Outline each blood parasite and name the species.
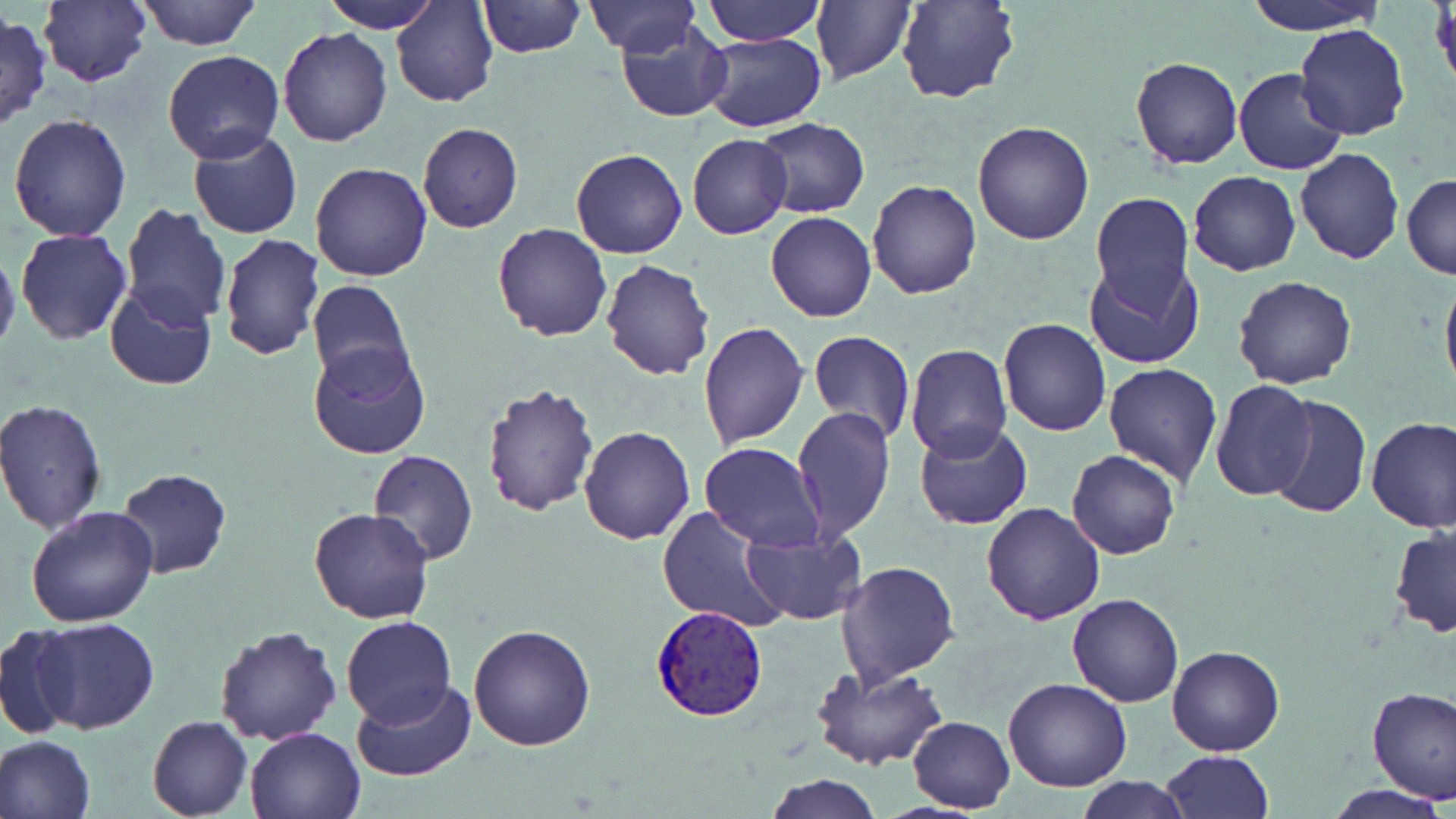
Approximate bounding boxes as (x1, y1, x2, y2) in pixels.
Plasmodium vivax-infected red blood cells: (649, 605, 770, 721).
No Plasmodium falciparum, Plasmodium ovale, Plasmodium malariae, Babesia divergens, or Trypanosoma brucei observed.

slide-level diagnosis = Plasmodium vivax
uninfected red blood cell locations = approximate bounding boxes as (x1, y1, x2, y2) in pixels: (134, 0, 263, 50), (322, 0, 440, 33), (393, 0, 497, 106), (477, 0, 586, 56), (703, 0, 825, 46), (811, 0, 917, 84), (897, 0, 1019, 105), (1242, 0, 1385, 34), (38, 1, 151, 86), (584, 1, 702, 56), (1, 12, 50, 130), (616, 20, 733, 123), (1295, 24, 1411, 140), (278, 29, 393, 147), (698, 33, 827, 132), (162, 50, 286, 165), (1130, 56, 1244, 169), (1232, 66, 1347, 175), (8, 113, 133, 242), (752, 118, 870, 217), (972, 120, 1094, 245), (418, 122, 524, 233), (187, 130, 303, 240), (688, 134, 793, 239), (569, 148, 688, 259), (1294, 148, 1404, 264), (310, 162, 433, 282), (1187, 170, 1301, 276), (1401, 174, 1455, 279), (867, 178, 981, 299), (1090, 193, 1197, 316), (121, 204, 229, 327), (765, 211, 876, 321), (493, 222, 613, 342), (15, 228, 132, 344), (218, 235, 325, 360), (0, 243, 20, 361), (1083, 256, 1204, 370), (600, 259, 715, 380), (1440, 268, 1456, 401), (1233, 275, 1356, 389), (306, 280, 415, 390), (104, 282, 217, 389), (999, 317, 1110, 436), (697, 322, 810, 449), (807, 329, 915, 444), (308, 340, 432, 461), (904, 344, 1012, 463), (1103, 362, 1223, 486), (1210, 380, 1317, 501), (480, 382, 600, 517), (1265, 394, 1370, 521), (0, 398, 108, 535), (792, 408, 894, 540), (1366, 415, 1456, 532), (913, 421, 1033, 531), (579, 425, 695, 545), (699, 442, 826, 551), (1067, 450, 1181, 559), (366, 451, 480, 566), (117, 469, 232, 579), (981, 502, 1106, 623), (26, 505, 159, 627), (656, 507, 788, 632), (309, 508, 435, 624), (1388, 526, 1456, 636), (740, 527, 867, 625), (837, 560, 959, 686), (1066, 594, 1185, 707), (1029, 610, 1177, 788), (340, 615, 456, 728), (32, 617, 159, 734), (468, 623, 597, 751), (214, 624, 343, 745), (1, 625, 82, 740), (1166, 644, 1284, 757), (812, 661, 949, 770), (1003, 677, 1131, 791), (351, 680, 473, 782), (1367, 685, 1456, 802), (146, 714, 252, 818), (907, 716, 1015, 812), (244, 725, 367, 818), (0, 734, 96, 819), (1158, 751, 1272, 819), (766, 774, 881, 818), (1076, 777, 1191, 817), (1326, 783, 1450, 818)
modality = light microscopy
preparation = thin blood film
stain = May-Grünwald-Giemsa
image size = 1456×819 pixels
field of view = single
magnification = 1000x